Locate every uninfected red blood cell.
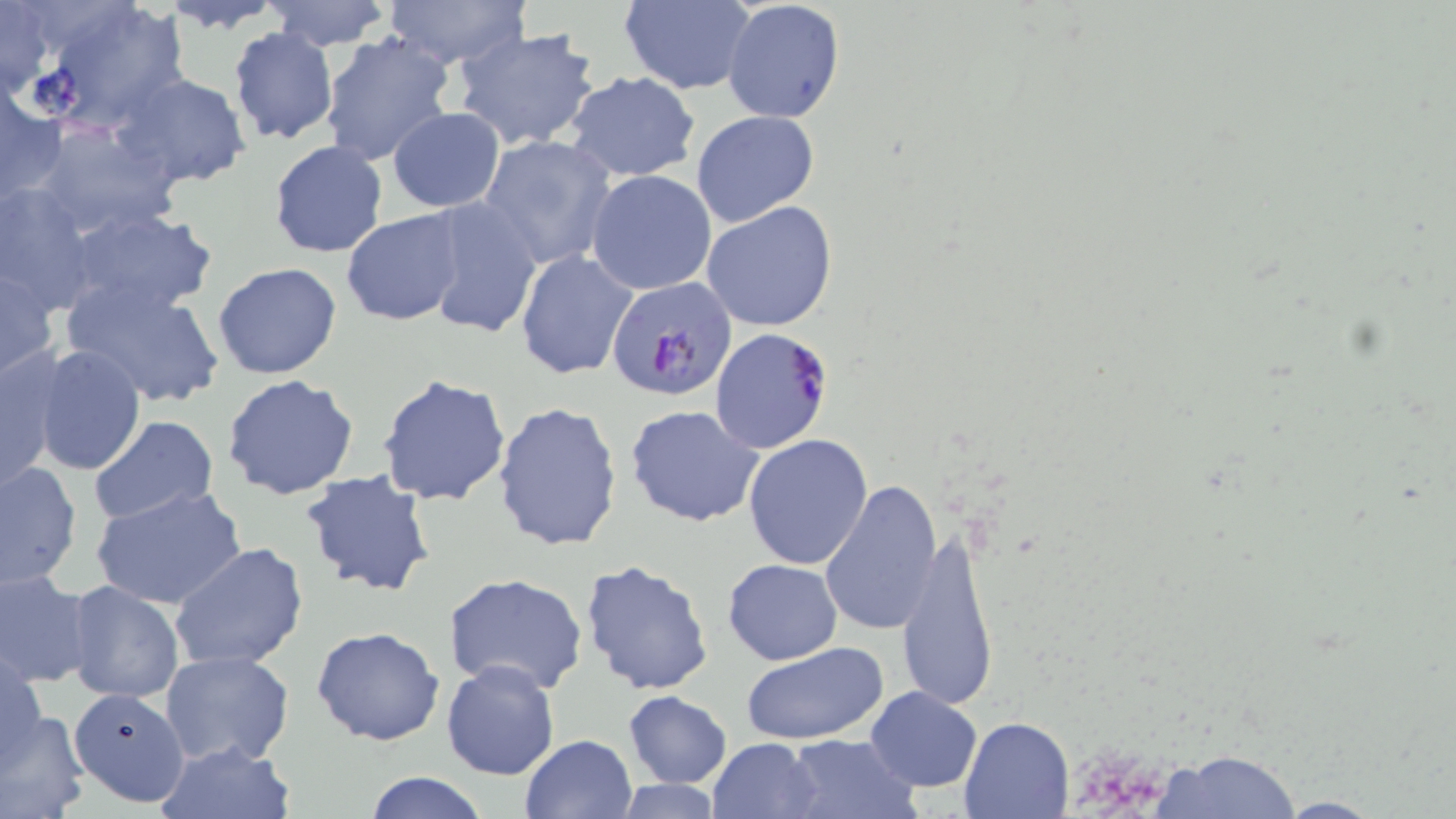
Approximate bounding boxes as named x1/y1/x2/y2 corners in pixels.
Uninfected red blood cells: (x1=155, y1=0, x2=285, y2=33), (x1=265, y1=0, x2=393, y2=50), (x1=383, y1=0, x2=531, y2=71), (x1=722, y1=0, x2=846, y2=124), (x1=0, y1=1, x2=54, y2=99), (x1=31, y1=1, x2=190, y2=134), (x1=618, y1=1, x2=756, y2=93), (x1=227, y1=27, x2=340, y2=147), (x1=453, y1=27, x2=602, y2=152), (x1=318, y1=31, x2=455, y2=169), (x1=113, y1=71, x2=251, y2=188), (x1=564, y1=71, x2=701, y2=183), (x1=1, y1=79, x2=64, y2=203), (x1=388, y1=107, x2=504, y2=212), (x1=692, y1=110, x2=820, y2=227), (x1=32, y1=120, x2=185, y2=239), (x1=480, y1=133, x2=617, y2=271), (x1=268, y1=139, x2=389, y2=259), (x1=586, y1=169, x2=718, y2=296), (x1=0, y1=183, x2=101, y2=317), (x1=420, y1=198, x2=543, y2=339), (x1=701, y1=201, x2=839, y2=332), (x1=60, y1=206, x2=218, y2=315), (x1=341, y1=210, x2=468, y2=327), (x1=515, y1=249, x2=638, y2=380), (x1=1, y1=262, x2=59, y2=381), (x1=212, y1=262, x2=343, y2=381), (x1=62, y1=277, x2=227, y2=409), (x1=31, y1=344, x2=147, y2=475), (x1=0, y1=346, x2=64, y2=493), (x1=378, y1=373, x2=512, y2=507), (x1=222, y1=375, x2=362, y2=501), (x1=492, y1=400, x2=624, y2=552), (x1=626, y1=403, x2=765, y2=528), (x1=88, y1=416, x2=220, y2=527), (x1=743, y1=434, x2=873, y2=570), (x1=1, y1=461, x2=81, y2=590), (x1=300, y1=469, x2=436, y2=597), (x1=818, y1=481, x2=943, y2=636), (x1=93, y1=486, x2=248, y2=611), (x1=893, y1=532, x2=1000, y2=712), (x1=169, y1=540, x2=309, y2=673), (x1=723, y1=557, x2=842, y2=666), (x1=577, y1=558, x2=715, y2=697), (x1=1, y1=569, x2=93, y2=689), (x1=442, y1=572, x2=591, y2=697), (x1=65, y1=580, x2=185, y2=705), (x1=311, y1=625, x2=446, y2=747), (x1=742, y1=643, x2=888, y2=747), (x1=1, y1=645, x2=47, y2=768), (x1=159, y1=650, x2=295, y2=769), (x1=440, y1=658, x2=562, y2=781), (x1=865, y1=686, x2=983, y2=793), (x1=72, y1=687, x2=191, y2=807), (x1=623, y1=691, x2=731, y2=788), (x1=0, y1=706, x2=91, y2=818), (x1=958, y1=716, x2=1072, y2=818), (x1=784, y1=732, x2=918, y2=818), (x1=517, y1=735, x2=637, y2=819), (x1=705, y1=737, x2=822, y2=818), (x1=152, y1=738, x2=297, y2=818), (x1=1155, y1=748, x2=1301, y2=818), (x1=361, y1=772, x2=490, y2=819), (x1=606, y1=779, x2=729, y2=817), (x1=1271, y1=795, x2=1384, y2=817).

Plasmodium falciparum-infected red blood cell locations: (x1=607, y1=278, x2=738, y2=401), (x1=709, y1=327, x2=833, y2=454). Slide-level diagnosis: Plasmodium falciparum. Optical microscopy. 1000x magnification. Image is 1456×819 pixels. Single field of view. May-Grünwald-Giemsa-stained preparation. Thin blood smear.